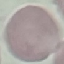
Malaria status: uninfected. Thin blood film. Acquired by smartphone through the microscope eyepiece. Cell patch, automatically extracted from a larger field of view and resized to 64 × 64 pixels. Giemsa-stained preparation.